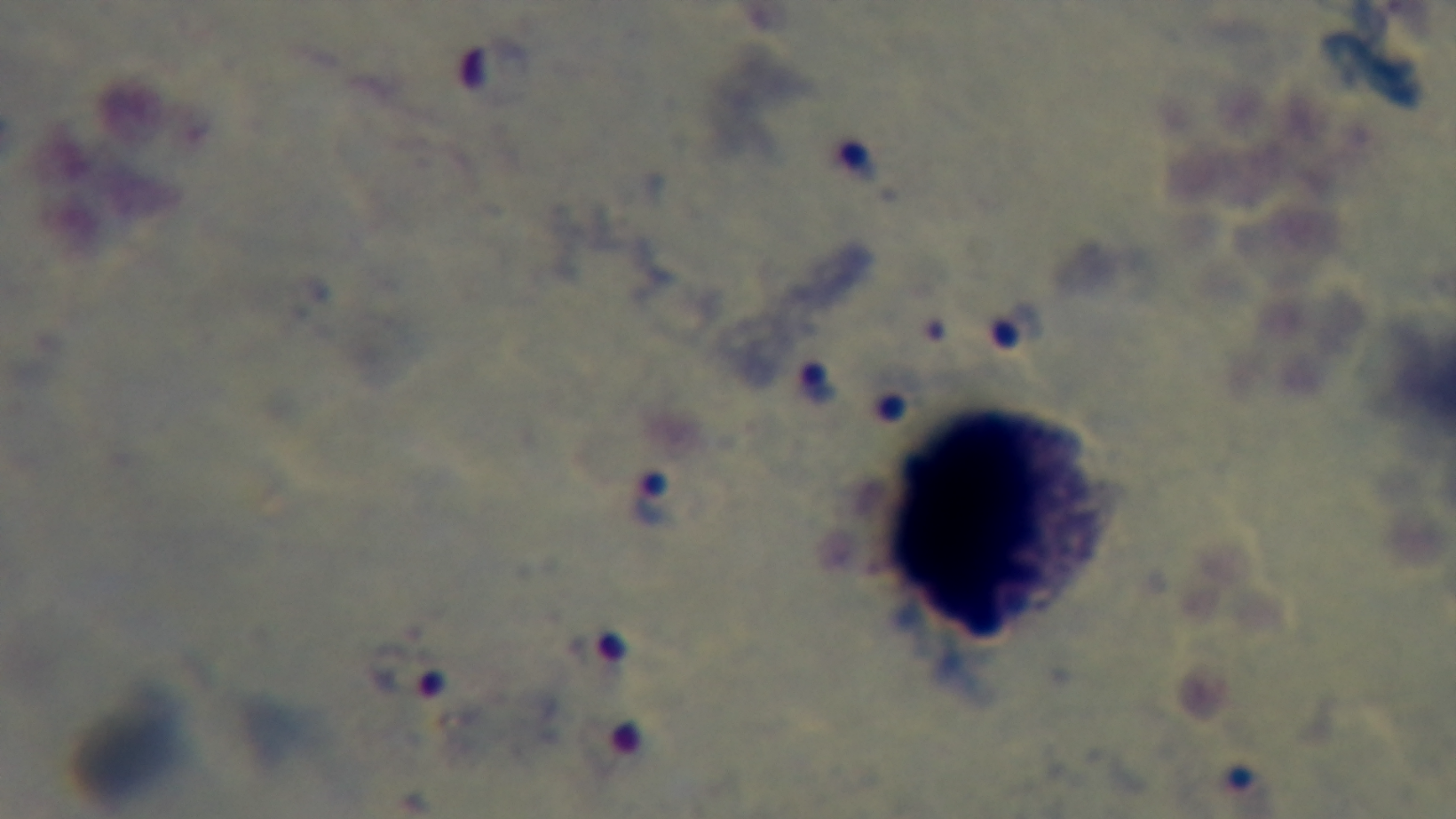 One field from the slide. Preparation: thick blood film. Captured with a mounted 4K digital camera. 100x oil-immersion objective. Malaria status: infected. Light microscopy. Giemsa-stained.